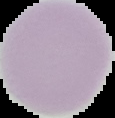

Summary:
  - Image size: 115×118 pixels
  - Result: negative for malaria parasites
  - Preparation: thin blood film
  - Image type: segmented cell region on a black background